Locate every blood parasite and identify its species.
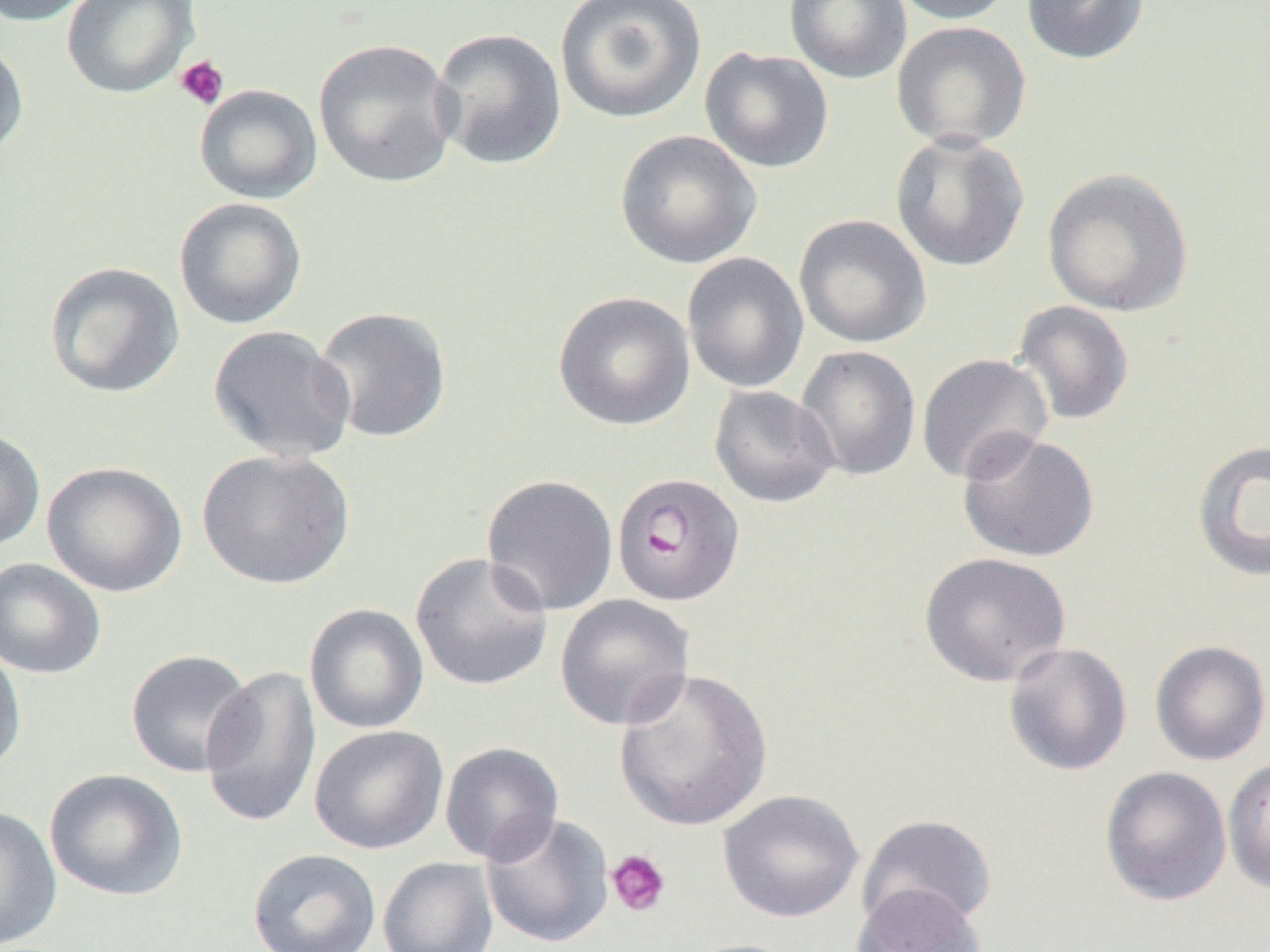

Approximate bounding boxes as [x1, y1, x2, y2] in pixels.
Plasmodium falciparum-infected red blood cells: [612, 472, 745, 606].
No Plasmodium ovale, Plasmodium malariae, Plasmodium vivax, Babesia divergens, or Trypanosoma brucei observed.

{
  "slide_level_diagnosis": "Plasmodium falciparum",
  "modality": "optical microscopy",
  "uninfected_red_blood_cell_locations": "approximate bounding boxes as [x1, y1, x2, y2] in pixels: [0, 0, 99, 26], [61, 0, 200, 98], [555, 0, 707, 124], [784, 0, 912, 85], [889, 0, 1016, 25], [1021, 0, 1149, 65], [891, 21, 1031, 151], [429, 26, 567, 170], [0, 38, 29, 164], [313, 38, 460, 189], [699, 47, 834, 174], [194, 84, 323, 204], [615, 130, 762, 269], [889, 131, 1031, 272], [1042, 167, 1194, 317], [174, 197, 307, 330], [794, 214, 931, 349], [682, 252, 809, 393], [43, 261, 186, 398], [553, 291, 696, 431], [1012, 301, 1135, 426], [312, 306, 453, 444], [207, 325, 356, 463], [795, 345, 922, 481], [916, 353, 1053, 484], [709, 385, 840, 508], [0, 428, 47, 552], [957, 430, 1100, 563], [1192, 439, 1270, 583], [197, 449, 355, 590], [42, 461, 188, 597], [481, 474, 619, 616], [411, 552, 554, 691], [919, 552, 1071, 687], [0, 557, 108, 679], [555, 594, 695, 731], [304, 604, 429, 734], [0, 640, 28, 778], [1150, 640, 1270, 765], [1003, 642, 1132, 776], [125, 649, 256, 778], [199, 664, 322, 831], [613, 667, 773, 832], [309, 725, 448, 854], [440, 742, 564, 865], [1223, 756, 1270, 895], [1099, 766, 1232, 907], [44, 768, 189, 902], [718, 789, 864, 923], [0, 804, 63, 951], [480, 813, 614, 949], [857, 814, 998, 932], [247, 848, 382, 952], [377, 857, 498, 952], [851, 883, 987, 952], [676, 938, 806, 952]",
  "platelet_locations": "approximate bounding boxes as [x1, y1, x2, y2] in pixels: [174, 54, 230, 110], [605, 849, 671, 918]",
  "preparation": "thin blood film",
  "field_of_view": "one of a larger specimen",
  "image_size": "1270×952 pixels",
  "magnification": "1000x"
}